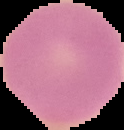

result = no malaria parasites detected
image type = segmented cell region with the area outside set to black
image size = 124×130 pixels
preparation = thin blood smear